Assess this cell for malaria.
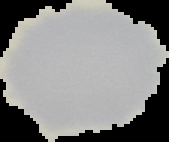
Uninfected.

From a thin blood film. The area outside the segmented cell region is set to black. Image is 169×142 pixels.